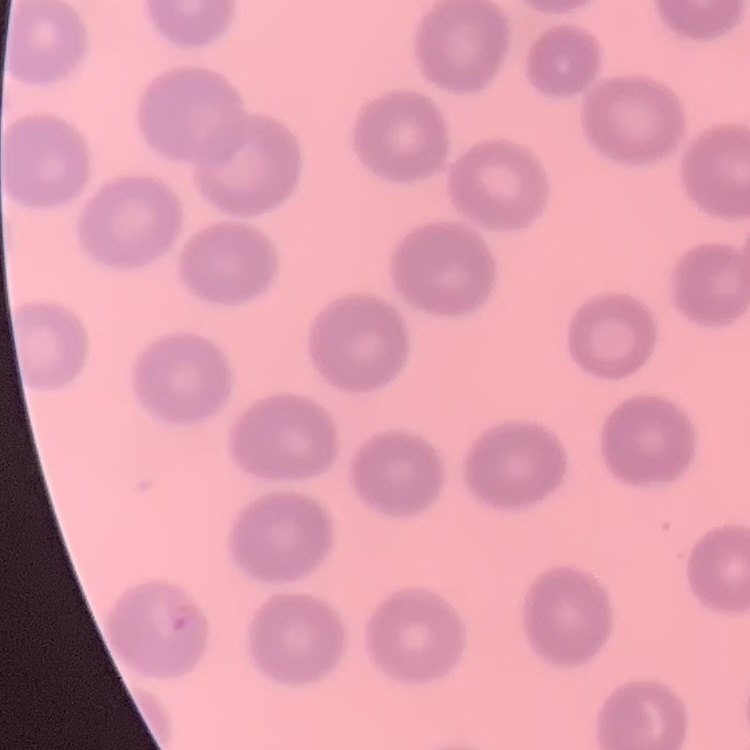

Summary:
  - Erythrocyte morphology: no rouleaux formation
  - Stain: Field's or Giemsa
  - Image type: square crop of a larger photomicrograph
  - Preparation: thin blood film